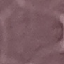

Malaria status: uninfected. Photographed with a smartphone camera at the microscope eyepiece. Cell patch, automatically extracted from a larger field of view and resized to 64 × 64 pixels. Giemsa stain. Thin blood film.